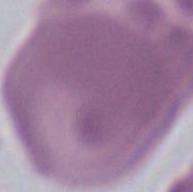
{
  "magnification": "1000x",
  "modality": "micrograph",
  "identification": "erythrocyte"
}